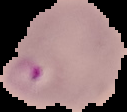 Malaria status: parasitized. From a thin blood film. Segmented cell region on a black background. Image is 127×112 pixels.